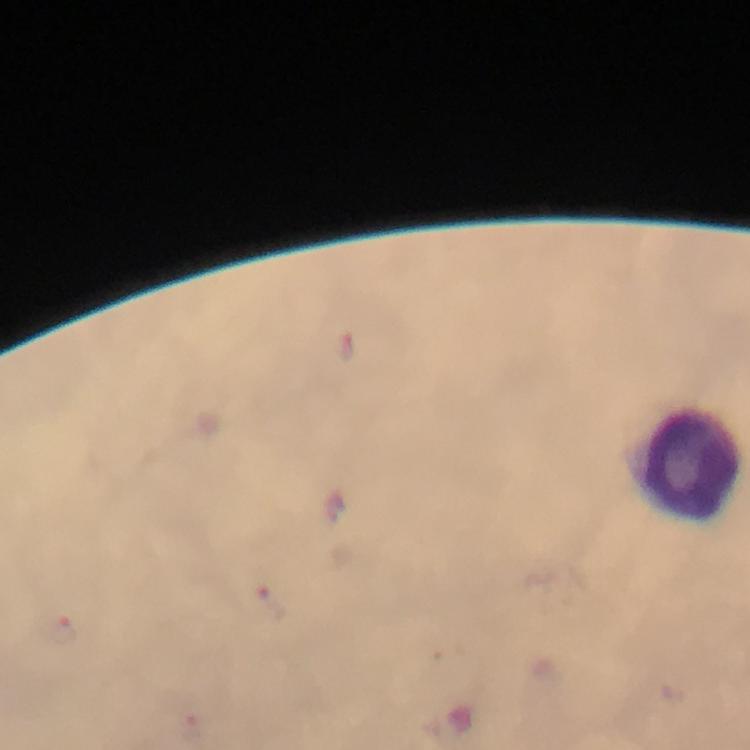

capture: smartphone photograph through a microscope
leukocyte_locations: 'approximate object centers, in pixels from the top-left corner: (x=688, y=463)'
image_size: 750×750 pixels
context: from a malaria diagnostic workup
cropped_from: one field of view
preparation: thick smear
immersion_oil: used
malaria_parasites: none detected
magnification: 100x
stain: Giemsa